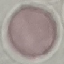
{
  "result": "no malaria parasites seen",
  "capture": "smartphone through the microscope eyepiece",
  "preparation": "thin blood smear",
  "stain": "Giemsa",
  "image_type": "cell patch, automatically extracted from a larger field of view and resized to 64 × 64 pixels"
}